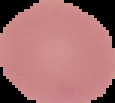

Summary:
  - Result: no Plasmodium parasites detected
  - Image size: 115×103 pixels
  - Image type: segmented cell region with the area outside set to black
  - Preparation: thin blood smear